Name the cell type shown.
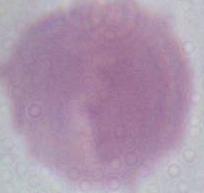
An erythrocyte.

modality: photomicrograph
magnification: 1000x